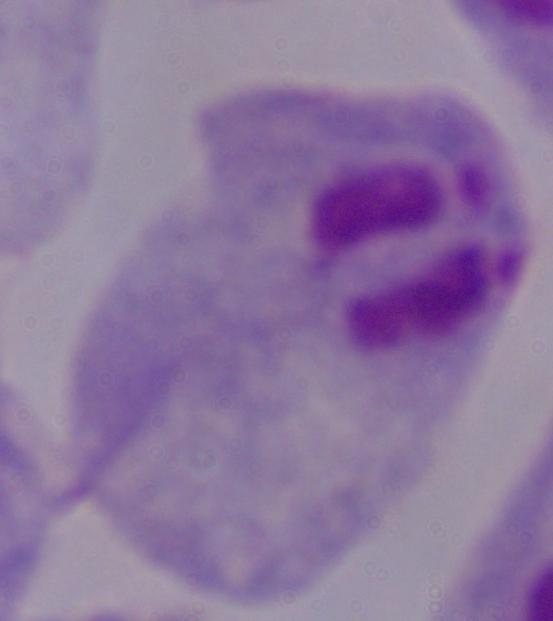

modality = photomicrograph
magnification = 1000x
identification = trichomonad